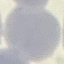
Summary:
  - Result: no malaria parasites seen
  - Capture: smartphone camera at the microscope eyepiece
  - Stain: Giemsa
  - Image type: cell patch, automatically extracted from a larger field of view and resized to 64 × 64 pixels
  - Preparation: thin blood film